Report the malaria status of this cell.
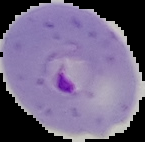
It is parasitized.

Image is 145×142 pixels. From a thin blood film. The area outside the segmented cell region is set to black.